Describe the morphology of the erythrocytes.
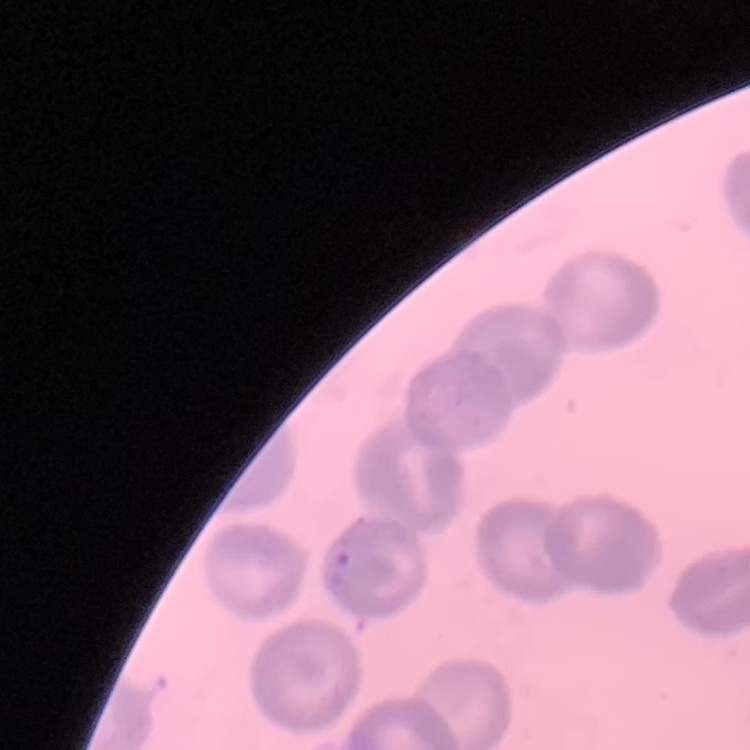

They show no rouleaux formation.

Summary:
  - Preparation: thin blood film
  - Image type: one tile cut from a larger photomicrograph
  - Stain: Field's or Giemsa